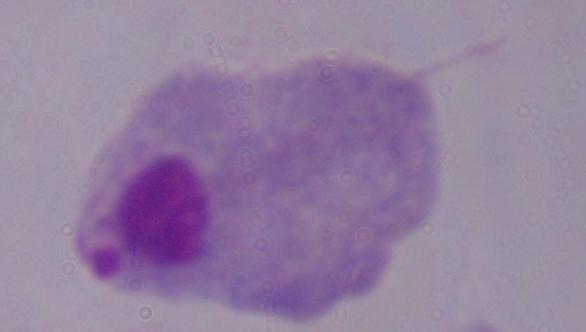
identification = trichomonad
modality = micrograph
magnification = 1000x